Evaluate for parasitized red blood cells.
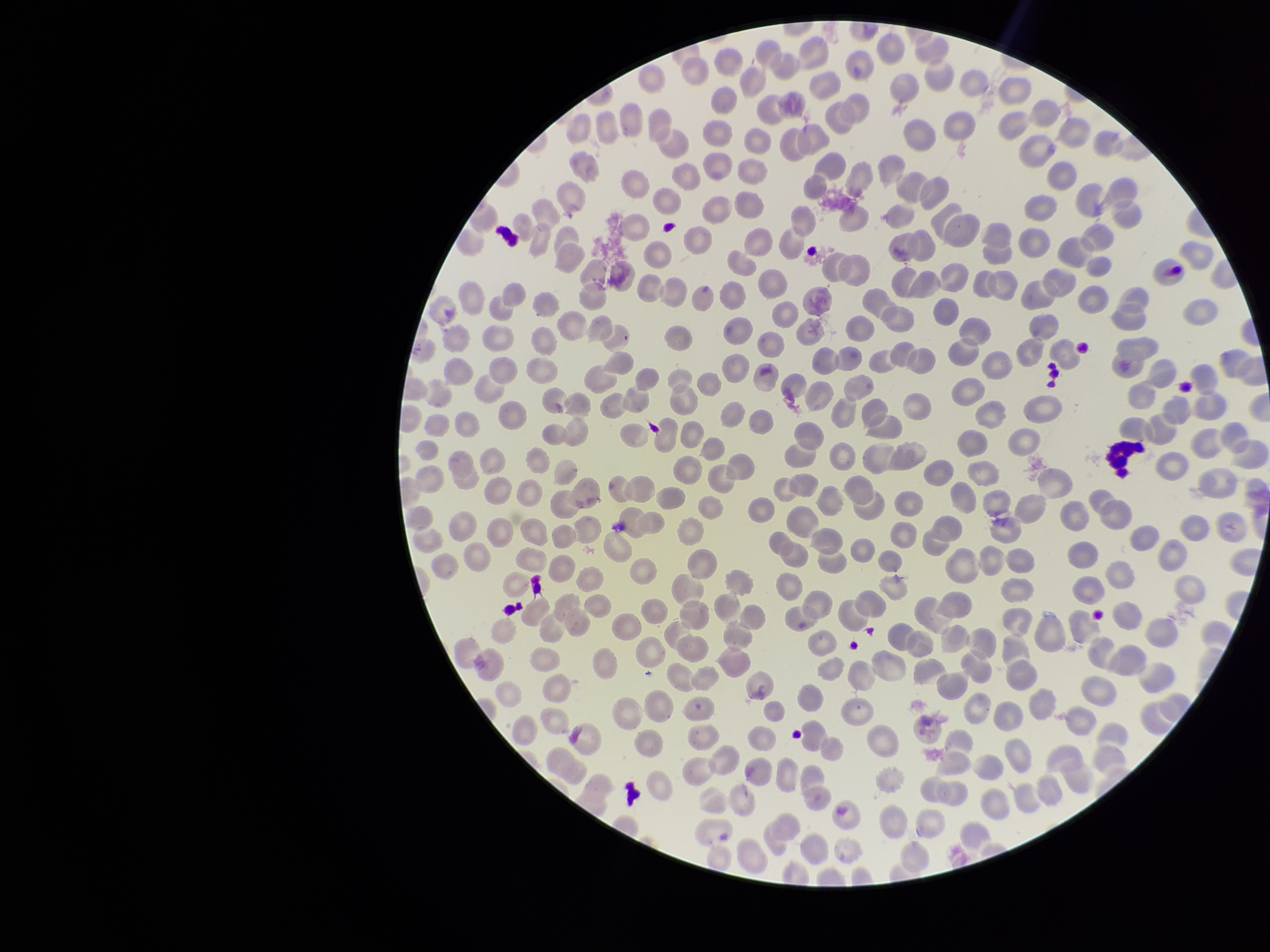
None identified.

Single field of view. Red blood cell count: 367. Image is 1270×952 pixels. Species reported for this patient: Plasmodium falciparum. Preparation: thin. Parasitized red blood cell count: 0. Stained with Giemsa. Smartphone photograph taken through the eyepiece of a microscope. Patient malaria status: infected.